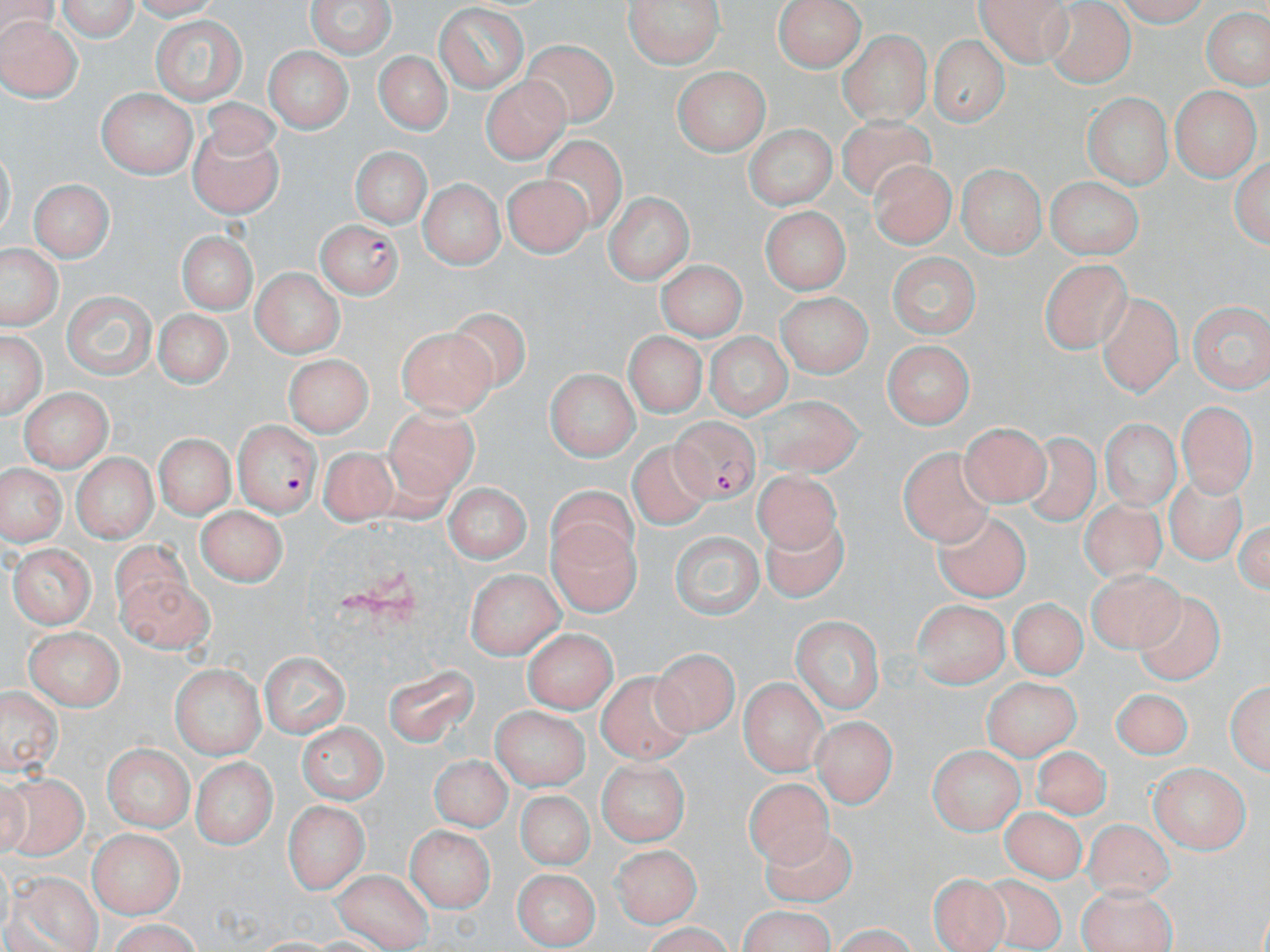
Approximate bounding boxes as named x1/y1/x2/y2 corners in pixels. Plasmodium falciparum-infected red blood cell locations: (x1=314, y1=221, x2=401, y2=298), (x1=231, y1=420, x2=318, y2=514), (x1=669, y1=420, x2=761, y2=506). Uninfected red blood cell locations: (x1=56, y1=0, x2=138, y2=43), (x1=303, y1=0, x2=400, y2=59), (x1=620, y1=0, x2=726, y2=66), (x1=772, y1=0, x2=869, y2=70), (x1=973, y1=0, x2=1073, y2=64), (x1=1111, y1=0, x2=1214, y2=25), (x1=1044, y1=4, x2=1133, y2=85), (x1=434, y1=6, x2=530, y2=89), (x1=1206, y1=12, x2=1269, y2=88), (x1=153, y1=16, x2=246, y2=106), (x1=0, y1=17, x2=80, y2=102), (x1=841, y1=29, x2=929, y2=122), (x1=516, y1=36, x2=620, y2=130), (x1=931, y1=37, x2=1012, y2=122), (x1=262, y1=46, x2=351, y2=135), (x1=374, y1=46, x2=452, y2=133), (x1=672, y1=66, x2=771, y2=152), (x1=481, y1=75, x2=569, y2=164), (x1=1170, y1=85, x2=1256, y2=181), (x1=99, y1=89, x2=197, y2=177), (x1=1087, y1=97, x2=1168, y2=187), (x1=835, y1=115, x2=938, y2=203), (x1=746, y1=118, x2=837, y2=214), (x1=188, y1=120, x2=287, y2=219), (x1=540, y1=136, x2=632, y2=235), (x1=346, y1=144, x2=436, y2=233), (x1=1231, y1=156, x2=1268, y2=251), (x1=871, y1=159, x2=956, y2=251), (x1=958, y1=167, x2=1041, y2=259), (x1=506, y1=172, x2=591, y2=254), (x1=1046, y1=177, x2=1144, y2=259), (x1=31, y1=181, x2=112, y2=261), (x1=417, y1=181, x2=503, y2=268), (x1=606, y1=193, x2=691, y2=285), (x1=762, y1=207, x2=848, y2=296), (x1=175, y1=230, x2=260, y2=312), (x1=3, y1=251, x2=58, y2=329), (x1=891, y1=254, x2=981, y2=338), (x1=1041, y1=257, x2=1131, y2=349), (x1=651, y1=260, x2=750, y2=347), (x1=251, y1=267, x2=339, y2=360), (x1=62, y1=289, x2=158, y2=379), (x1=774, y1=292, x2=864, y2=372), (x1=1097, y1=297, x2=1189, y2=401), (x1=1188, y1=300, x2=1269, y2=394), (x1=151, y1=304, x2=227, y2=382), (x1=452, y1=306, x2=536, y2=395), (x1=397, y1=324, x2=498, y2=413), (x1=0, y1=325, x2=45, y2=425), (x1=703, y1=331, x2=796, y2=416), (x1=612, y1=333, x2=713, y2=418), (x1=881, y1=338, x2=975, y2=426), (x1=285, y1=352, x2=369, y2=436), (x1=545, y1=369, x2=639, y2=458), (x1=18, y1=387, x2=113, y2=465), (x1=753, y1=395, x2=873, y2=485), (x1=1176, y1=398, x2=1253, y2=497), (x1=387, y1=406, x2=477, y2=504), (x1=1102, y1=417, x2=1180, y2=507), (x1=960, y1=421, x2=1049, y2=503), (x1=1013, y1=430, x2=1103, y2=528), (x1=153, y1=434, x2=238, y2=517), (x1=629, y1=441, x2=716, y2=523), (x1=895, y1=443, x2=995, y2=556), (x1=318, y1=444, x2=399, y2=531), (x1=70, y1=452, x2=156, y2=540), (x1=1, y1=461, x2=62, y2=547), (x1=1164, y1=470, x2=1246, y2=568), (x1=752, y1=473, x2=845, y2=556), (x1=443, y1=483, x2=530, y2=565), (x1=548, y1=487, x2=645, y2=573), (x1=1079, y1=498, x2=1170, y2=585), (x1=195, y1=507, x2=282, y2=587), (x1=762, y1=512, x2=853, y2=604), (x1=933, y1=512, x2=1031, y2=600), (x1=546, y1=515, x2=640, y2=620), (x1=673, y1=532, x2=765, y2=619), (x1=107, y1=537, x2=198, y2=618), (x1=9, y1=543, x2=96, y2=626), (x1=1087, y1=567, x2=1179, y2=652), (x1=466, y1=569, x2=559, y2=658), (x1=117, y1=573, x2=216, y2=659), (x1=1130, y1=592, x2=1233, y2=689), (x1=1009, y1=598, x2=1087, y2=674), (x1=912, y1=602, x2=1008, y2=688), (x1=793, y1=617, x2=882, y2=713), (x1=24, y1=627, x2=123, y2=708), (x1=523, y1=630, x2=617, y2=711), (x1=655, y1=646, x2=738, y2=734), (x1=258, y1=652, x2=347, y2=737), (x1=381, y1=661, x2=480, y2=748), (x1=171, y1=663, x2=264, y2=759), (x1=596, y1=670, x2=695, y2=762), (x1=1226, y1=674, x2=1268, y2=775), (x1=740, y1=675, x2=822, y2=775), (x1=983, y1=675, x2=1081, y2=762), (x1=1, y1=683, x2=62, y2=777), (x1=1110, y1=685, x2=1191, y2=762), (x1=488, y1=705, x2=591, y2=788), (x1=812, y1=716, x2=894, y2=807), (x1=296, y1=721, x2=390, y2=801), (x1=102, y1=743, x2=193, y2=830), (x1=928, y1=743, x2=1024, y2=833), (x1=1031, y1=745, x2=1110, y2=817), (x1=429, y1=755, x2=510, y2=832), (x1=193, y1=756, x2=272, y2=849), (x1=597, y1=761, x2=686, y2=844), (x1=1151, y1=763, x2=1248, y2=853), (x1=747, y1=771, x2=837, y2=871), (x1=1, y1=772, x2=89, y2=864), (x1=513, y1=788, x2=602, y2=868), (x1=283, y1=801, x2=366, y2=893), (x1=1000, y1=807, x2=1088, y2=879), (x1=1078, y1=818, x2=1185, y2=906), (x1=761, y1=825, x2=876, y2=906), (x1=407, y1=826, x2=494, y2=913), (x1=86, y1=829, x2=184, y2=916), (x1=607, y1=838, x2=697, y2=925), (x1=333, y1=867, x2=432, y2=951), (x1=512, y1=869, x2=601, y2=947), (x1=12, y1=871, x2=101, y2=952), (x1=927, y1=873, x2=1018, y2=952), (x1=979, y1=874, x2=1068, y2=947), (x1=1079, y1=885, x2=1178, y2=952), (x1=738, y1=907, x2=834, y2=952), (x1=98, y1=920, x2=203, y2=951). Slide-level diagnosis: Plasmodium falciparum. Thin blood smear. 1000x magnification. Optical microscopy. Image is 1270×952 pixels. May-Grünwald-Giemsa-stained preparation. One field of a larger specimen.